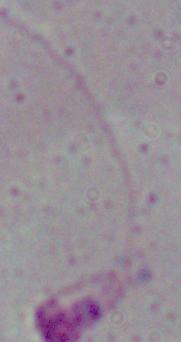

{
  "identification": "Leishmania",
  "magnification": "1000x",
  "modality": "micrograph"
}